State the blood parasite species.
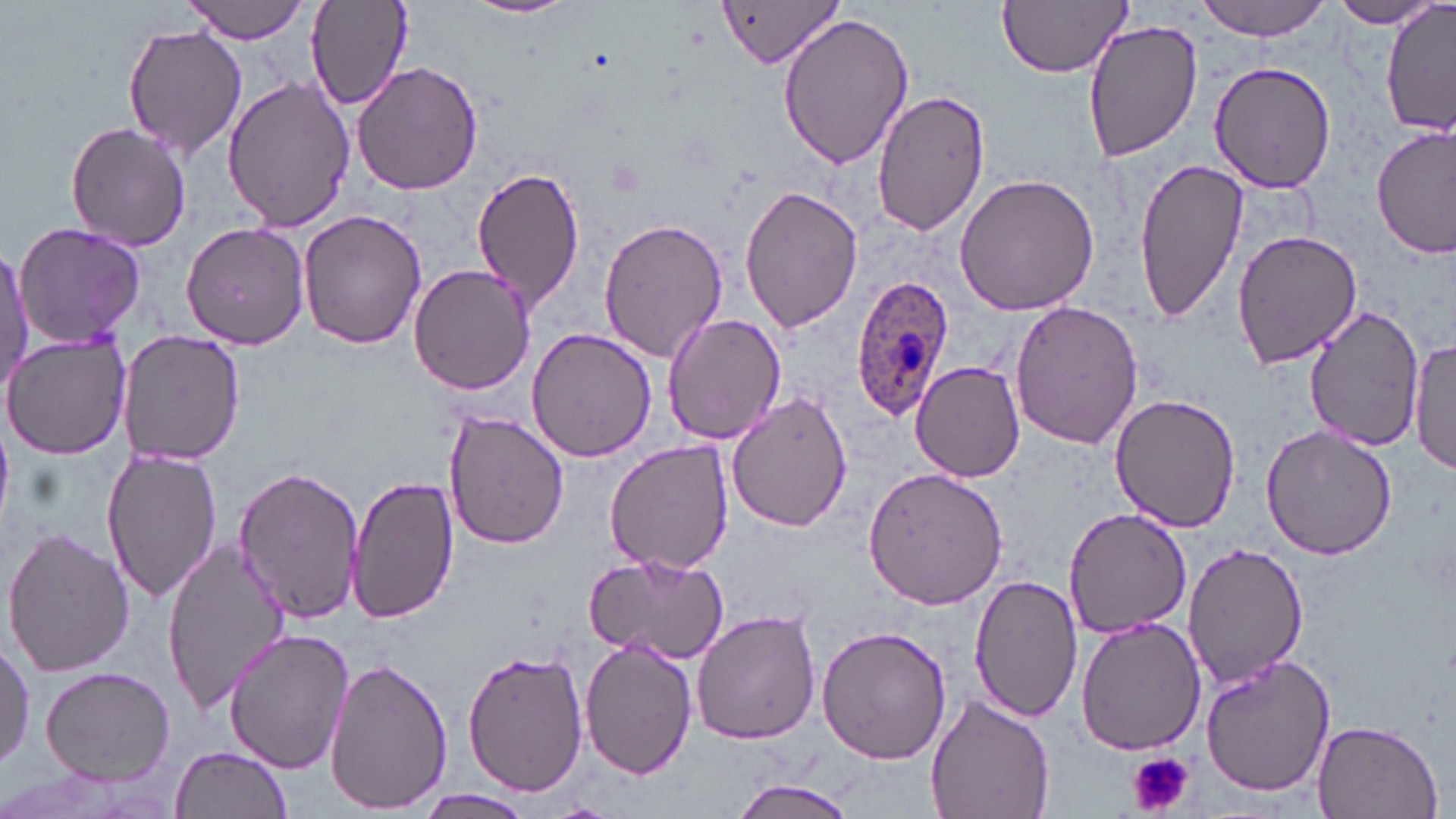
Plasmodium ovale.

Summary:
  - Coordinate format: approximate bounding boxes as (x1, y1, x2, y2) in pixels
  - Platelet locations: (1128, 751, 1194, 818)
  - Uninfected red blood cell locations: (305, 0, 413, 115), (465, 0, 578, 20), (719, 0, 847, 70), (999, 0, 1133, 78), (1194, 0, 1332, 40), (181, 1, 313, 44), (1325, 1, 1445, 29), (1382, 2, 1455, 139), (777, 10, 914, 169), (1081, 17, 1201, 162), (122, 24, 250, 158), (354, 60, 484, 195), (1208, 61, 1339, 193), (223, 75, 356, 232), (873, 86, 991, 237), (64, 121, 192, 251), (1373, 124, 1455, 260), (1133, 158, 1248, 322), (469, 165, 588, 312), (955, 171, 1100, 312), (739, 183, 866, 334), (298, 208, 426, 349), (597, 218, 731, 362), (182, 220, 310, 349), (12, 222, 147, 349), (1232, 229, 1362, 369), (0, 246, 33, 391), (408, 264, 536, 395), (1010, 301, 1144, 450), (1303, 305, 1425, 453), (661, 312, 786, 447), (526, 330, 659, 464), (2, 332, 134, 461), (118, 333, 243, 466), (1411, 336, 1455, 478), (912, 361, 1025, 481), (726, 389, 854, 530), (1108, 391, 1243, 530), (445, 411, 569, 550), (1262, 425, 1397, 561), (603, 438, 732, 576), (100, 448, 220, 603), (232, 465, 366, 624), (864, 468, 1008, 610), (347, 474, 459, 625), (1061, 509, 1195, 638), (2, 525, 134, 679), (162, 535, 295, 714), (1180, 543, 1309, 688), (584, 551, 731, 666), (970, 574, 1084, 724), (692, 608, 823, 744), (1074, 618, 1207, 757), (814, 624, 952, 765), (225, 629, 353, 773), (1, 633, 32, 777), (583, 639, 698, 780), (460, 650, 586, 797), (1203, 654, 1337, 797), (325, 658, 452, 816), (39, 667, 174, 785), (925, 696, 1057, 819), (1311, 718, 1443, 819), (170, 745, 293, 819), (729, 777, 861, 819), (411, 790, 536, 818)
  - Plasmodium ovale-infected red blood cell locations: (850, 274, 956, 420)
  - Magnification: 1000x
  - Image size: 1456×819 pixels
  - Field of view: single
  - Preparation: thin blood smear
  - Modality: optical microscopy
  - Stain: May-Grünwald-Giemsa